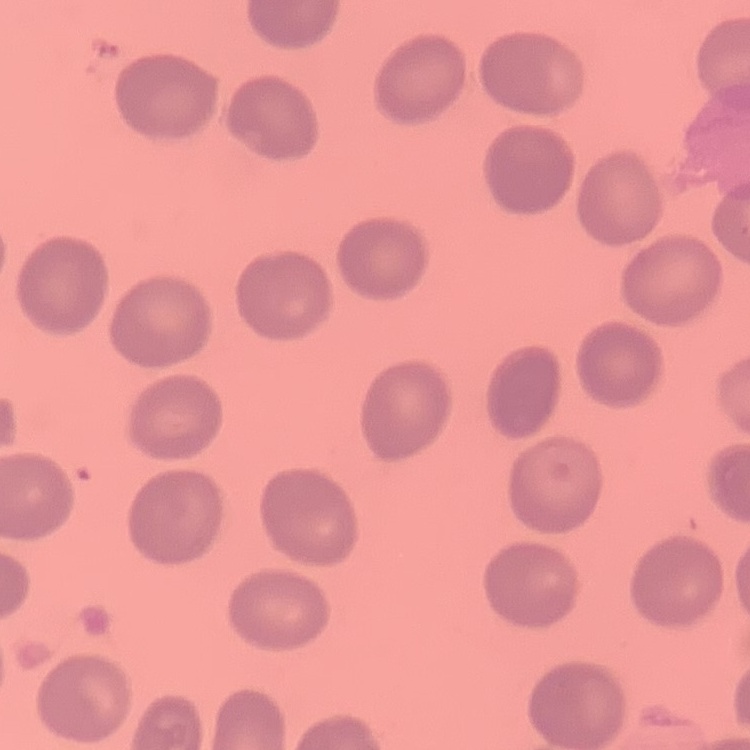
The red blood cells exhibit no rouleaux formation. Stained with either Field's or Giemsa. Thin blood film. Square crop of a larger photomicrograph.